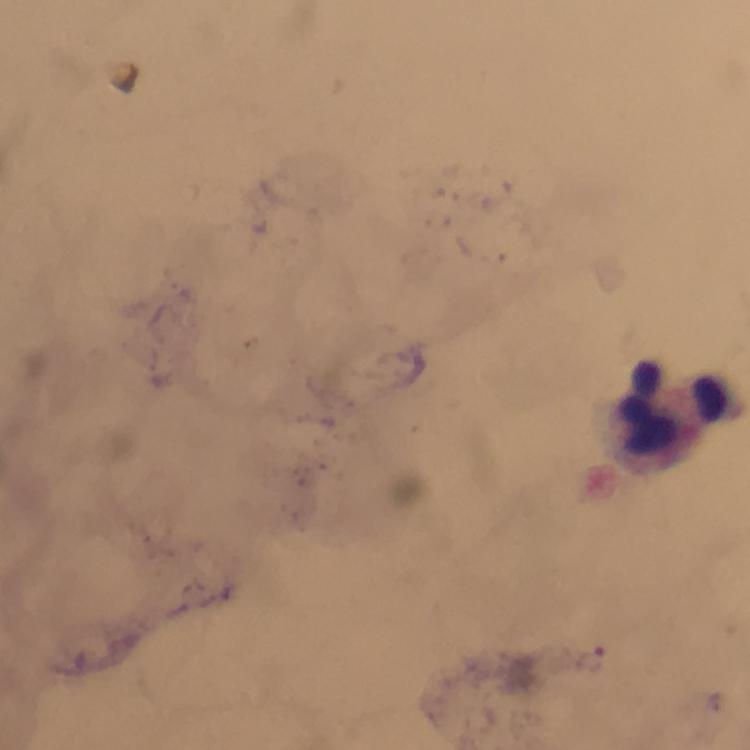

Approximate centers as [x, y] in pixels.
Summary:
  - Leukocyte locations: [675, 413]
  - Malaria parasite locations: [589, 658]
  - Context: from a malaria diagnostic workup
  - Stain: Giemsa
  - Image size: 750×750 pixels
  - Capture: smartphone mounted on the microscope
  - Immersion oil: used
  - Magnification: 100x
  - Preparation: thick blood smear
  - Cropped from: one field of view